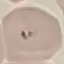

Summary:
  - Result: malaria parasites identified
  - Image type: automatically extracted cell patch, resized to 64 × 64 pixels
  - Capture: smartphone through the microscope eyepiece
  - Stain: Giemsa
  - Preparation: thin blood smear